Assess this cell for malaria.
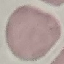
It is uninfected.

Acquired by smartphone through the microscope eyepiece. Giemsa stain. Thin blood film. Automatically extracted cell patch, resized to 64 × 64 pixels.